Assess for Plasmodium parasites.
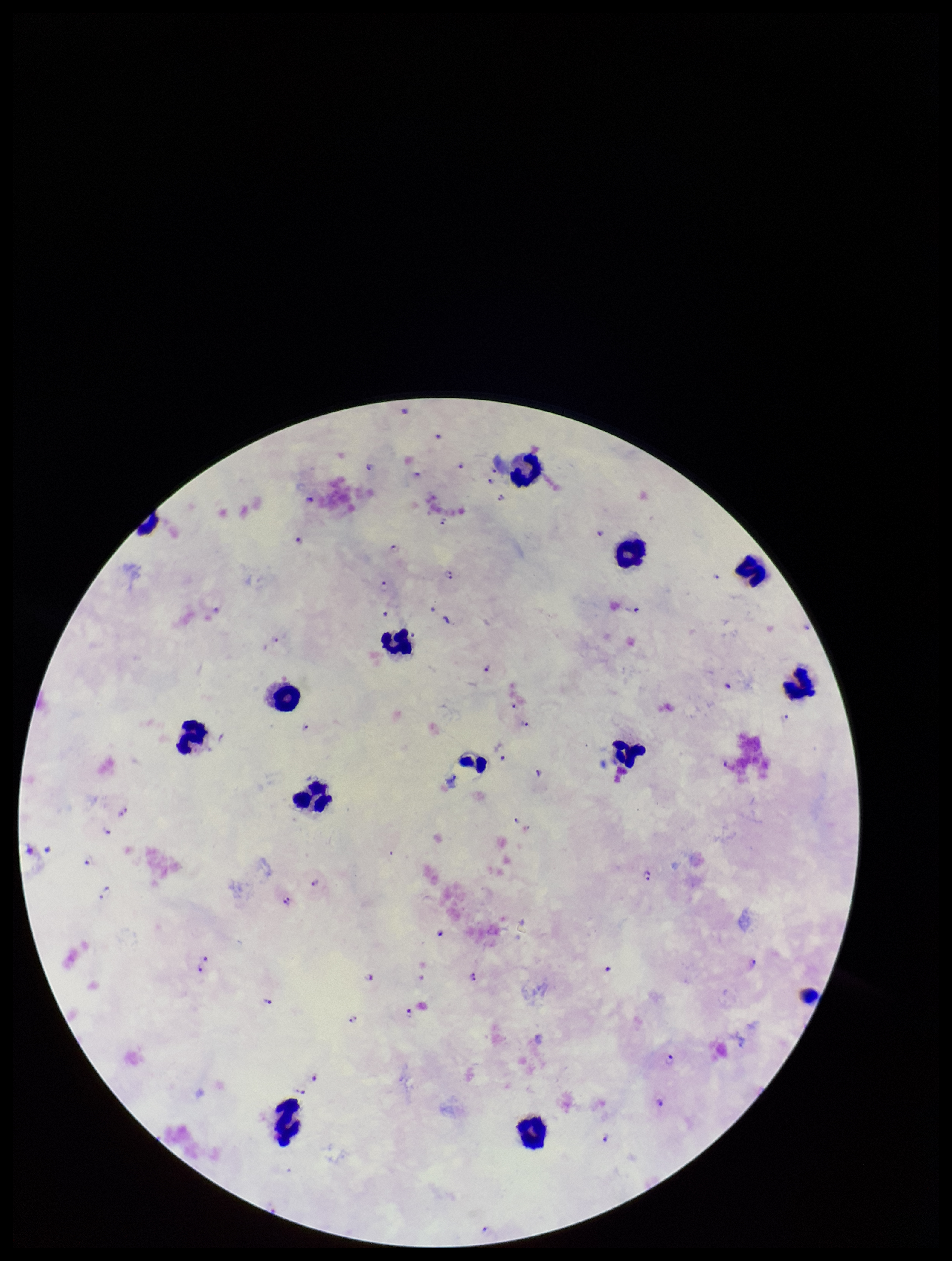

Seen.

stain = Giemsa
parasite count = 42
preparation = thick blood smear
leukocyte count = 13
species reported for this patient = Plasmodium falciparum
field of view = single
capture = smartphone photograph through the microscope eyepiece
image size = 952×1261 pixels
patient malaria status = infected